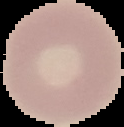 Image is 124×127 pixels. From a thin blood film. Segmented cell region on a black background. Malaria status: uninfected.